Report the malaria status of this cell.
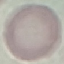
Uninfected.

Summary:
  - Preparation: thin blood smear
  - Image type: automatically extracted cell patch, resized to 64 × 64 pixels
  - Capture: smartphone camera at the microscope eyepiece
  - Stain: Giemsa